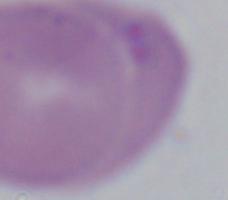

Micrograph. Captured at 1000x magnification. A Babesia parasite is shown.